Comment on the morphology of the red blood cells.
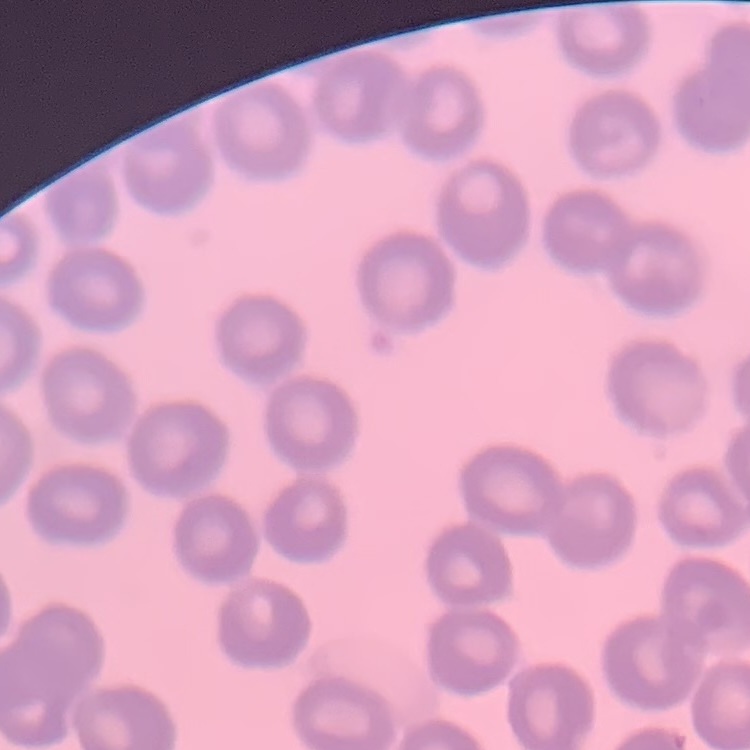

They show no rouleaux formation.

Summary:
  - Stain: Field's or Giemsa
  - Preparation: thin blood film
  - Image type: square crop of a larger photomicrograph